Describe the morphology of the erythrocytes.
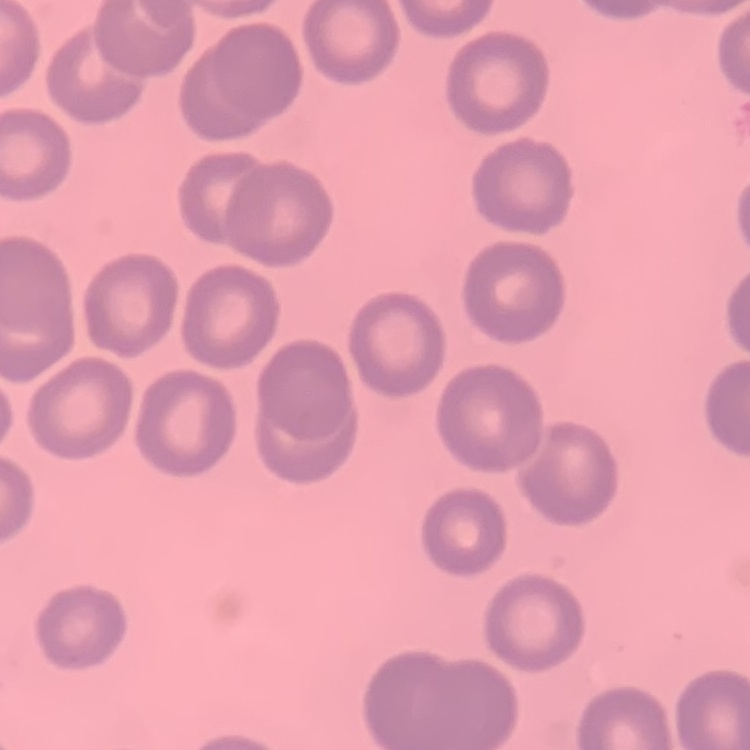

They show no rouleaux formation.

Summary:
  - Preparation: thin blood smear
  - Image type: square crop of a larger photomicrograph
  - Stain: Field's or Giemsa